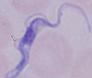

Captured at 1000x magnification. Micrograph. A trypanosome is shown.